Assess this cell for malaria.
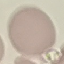
It is uninfected.

stain = Giemsa
image type = automatically extracted cell patch, resized to 64 × 64 pixels
preparation = thin blood film
capture = smartphone camera at the microscope eyepiece